Identify the blood parasite species.
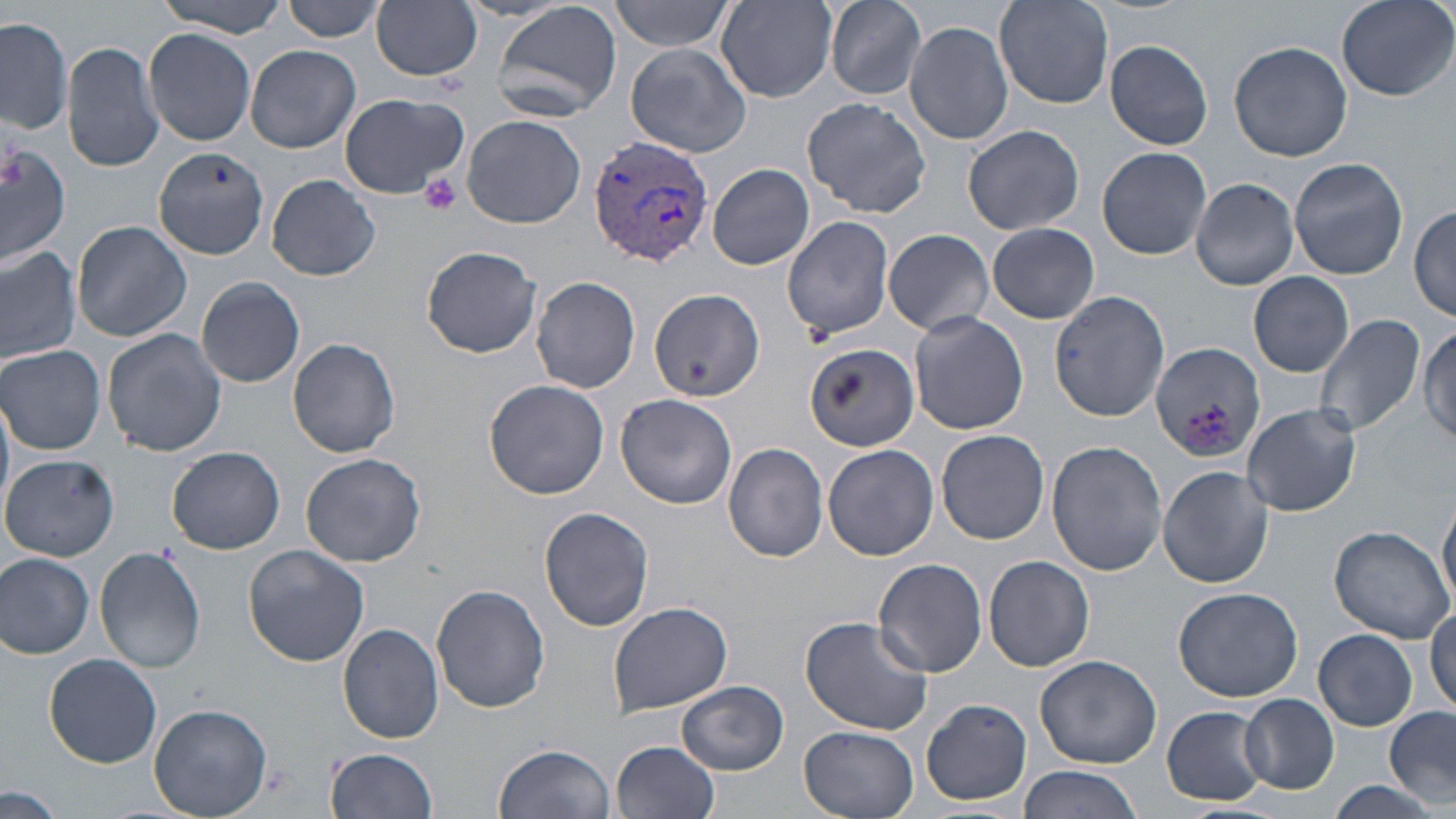

Plasmodium vivax.

Summary:
  - Coordinate format: approximate bounding boxes as named x1/y1/x2/y2 corners in pixels
  - Plasmodium vivax-infected red blood cell locations: (x1=588, y1=135, x2=713, y2=268)
  - Uninfected red blood cell locations: (x1=153, y1=0, x2=290, y2=36), (x1=285, y1=0, x2=388, y2=42), (x1=826, y1=0, x2=929, y2=100), (x1=993, y1=0, x2=1114, y2=111), (x1=1336, y1=0, x2=1454, y2=101), (x1=491, y1=1, x2=623, y2=121), (x1=611, y1=1, x2=736, y2=52), (x1=717, y1=1, x2=837, y2=100), (x1=372, y1=2, x2=483, y2=81), (x1=0, y1=15, x2=74, y2=135), (x1=903, y1=20, x2=1013, y2=144), (x1=144, y1=28, x2=257, y2=145), (x1=62, y1=39, x2=165, y2=173), (x1=1106, y1=39, x2=1213, y2=149), (x1=1229, y1=41, x2=1352, y2=161), (x1=626, y1=43, x2=752, y2=157), (x1=244, y1=45, x2=361, y2=153), (x1=338, y1=92, x2=469, y2=199), (x1=801, y1=97, x2=931, y2=217), (x1=461, y1=114, x2=586, y2=228), (x1=963, y1=124, x2=1084, y2=236), (x1=0, y1=139, x2=73, y2=269), (x1=1098, y1=145, x2=1212, y2=259), (x1=152, y1=148, x2=269, y2=259), (x1=1288, y1=157, x2=1410, y2=279), (x1=708, y1=163, x2=813, y2=271), (x1=262, y1=175, x2=382, y2=280), (x1=1189, y1=177, x2=1299, y2=292), (x1=1410, y1=204, x2=1456, y2=323), (x1=782, y1=213, x2=896, y2=341), (x1=72, y1=220, x2=191, y2=342), (x1=987, y1=223, x2=1100, y2=324), (x1=882, y1=228, x2=994, y2=337), (x1=420, y1=245, x2=543, y2=357), (x1=0, y1=247, x2=81, y2=365), (x1=1248, y1=271, x2=1354, y2=377), (x1=196, y1=277, x2=306, y2=389), (x1=531, y1=277, x2=641, y2=393), (x1=649, y1=287, x2=764, y2=402), (x1=1051, y1=289, x2=1169, y2=420), (x1=909, y1=311, x2=1028, y2=435), (x1=1313, y1=313, x2=1425, y2=438), (x1=1419, y1=320, x2=1456, y2=450), (x1=102, y1=327, x2=227, y2=457), (x1=287, y1=337, x2=401, y2=459), (x1=1150, y1=341, x2=1258, y2=462), (x1=804, y1=342, x2=919, y2=451), (x1=0, y1=344, x2=107, y2=455), (x1=483, y1=379, x2=610, y2=500), (x1=0, y1=391, x2=14, y2=518), (x1=616, y1=394, x2=737, y2=509), (x1=1242, y1=403, x2=1360, y2=517), (x1=936, y1=429, x2=1050, y2=545), (x1=1045, y1=440, x2=1166, y2=578), (x1=722, y1=443, x2=829, y2=562), (x1=823, y1=444, x2=939, y2=562), (x1=168, y1=446, x2=287, y2=553), (x1=300, y1=452, x2=426, y2=568), (x1=2, y1=453, x2=119, y2=562), (x1=1158, y1=466, x2=1274, y2=587), (x1=1438, y1=499, x2=1456, y2=612), (x1=538, y1=506, x2=654, y2=632), (x1=1327, y1=524, x2=1453, y2=643), (x1=243, y1=544, x2=369, y2=667), (x1=93, y1=549, x2=207, y2=674), (x1=0, y1=552, x2=93, y2=659), (x1=984, y1=555, x2=1095, y2=672), (x1=873, y1=559, x2=989, y2=678), (x1=431, y1=585, x2=550, y2=714), (x1=1172, y1=585, x2=1304, y2=701), (x1=607, y1=602, x2=731, y2=714), (x1=1427, y1=604, x2=1456, y2=714), (x1=800, y1=615, x2=933, y2=736), (x1=337, y1=623, x2=444, y2=744), (x1=1314, y1=629, x2=1418, y2=730), (x1=44, y1=653, x2=163, y2=767), (x1=1035, y1=654, x2=1162, y2=768), (x1=677, y1=680, x2=788, y2=775), (x1=1240, y1=694, x2=1339, y2=794), (x1=921, y1=699, x2=1031, y2=805), (x1=150, y1=703, x2=273, y2=818), (x1=1162, y1=706, x2=1268, y2=805), (x1=1383, y1=707, x2=1456, y2=806), (x1=798, y1=726, x2=920, y2=818), (x1=610, y1=740, x2=720, y2=818), (x1=494, y1=744, x2=614, y2=819), (x1=327, y1=748, x2=439, y2=818), (x1=1017, y1=764, x2=1145, y2=818), (x1=1325, y1=779, x2=1440, y2=818), (x1=0, y1=786, x2=62, y2=819)
  - Platelet locations: (x1=419, y1=174, x2=463, y2=216)
  - Preparation: thin blood film
  - Modality: optical microscopy
  - Magnification: 1000x
  - Field of view: single
  - Stain: May-Grünwald-Giemsa
  - Image size: 1456×819 pixels